Classify this cell by malaria status.
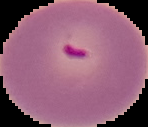
It is parasitized.

image size = 148×127 pixels
image type = segmented cell region with the area outside set to black
preparation = thin blood film